Identify the parasite.
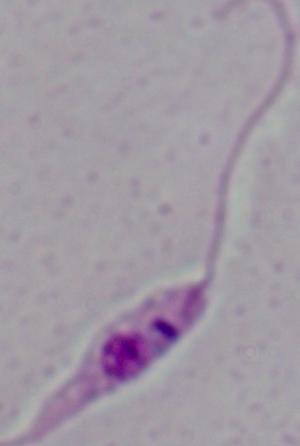
This is Leishmania.

modality = micrograph
magnification = 1000x